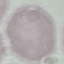

Summary:
  - Malaria status: uninfected
  - Capture: smartphone through the microscope eyepiece
  - Image type: automatically extracted cell patch, resized to 64 × 64 pixels
  - Preparation: thin blood film
  - Stain: Giemsa